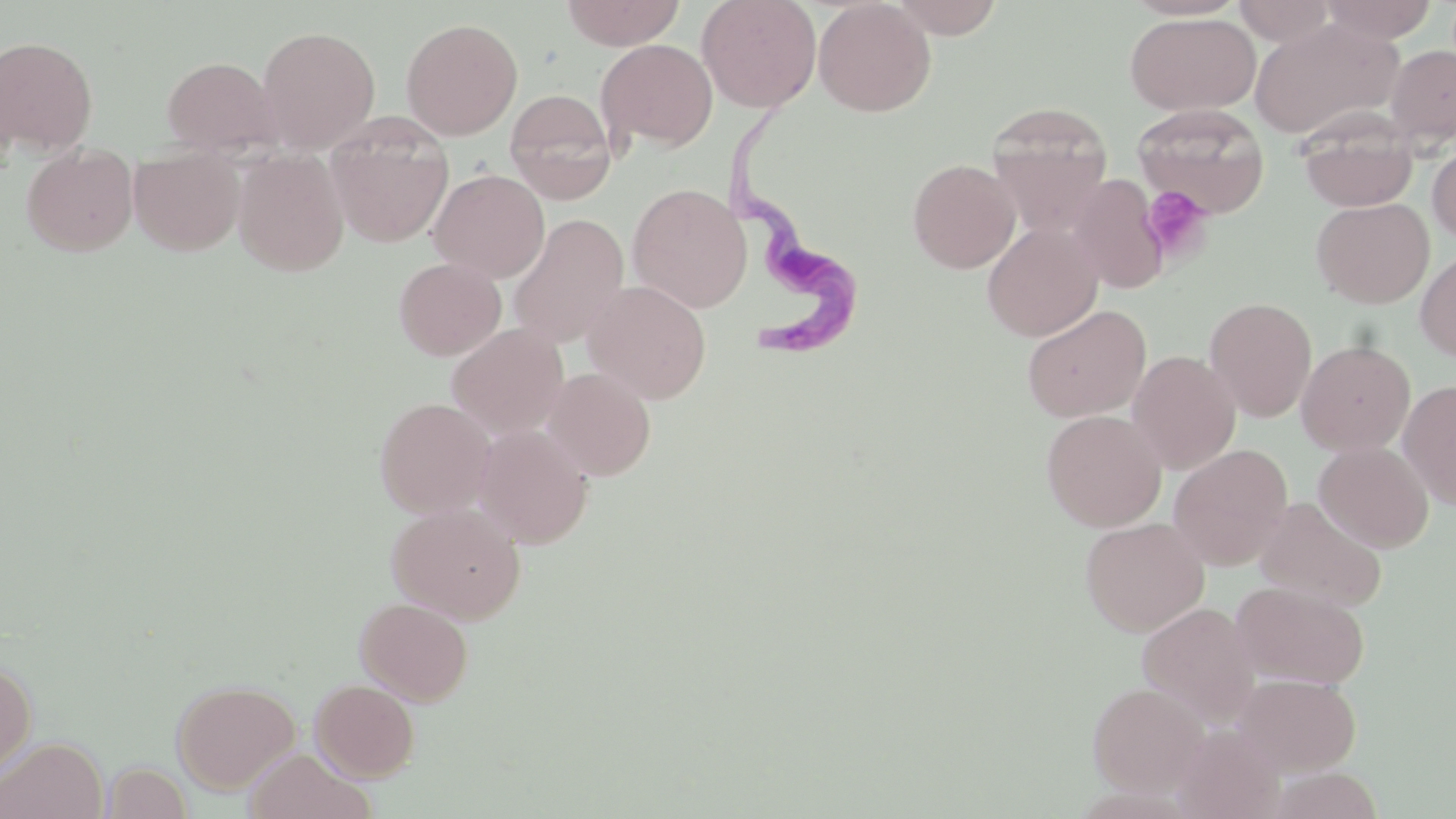
Summary:
  - Coordinate format: approximate bounding boxes as (x1,y1)-(x2,y2) corner pairs in pixels
  - Trypanosoma brucei locations: (720,118)-(870,367)
  - Platelet locations: (1140,184)-(1214,263)
  - Uninfected red blood cell locations: (561,0)-(686,50), (697,0)-(822,113), (813,0)-(936,117), (887,0)-(1006,38), (1231,0)-(1341,45), (1321,0)-(1440,43), (1125,12)-(1260,115), (400,17)-(523,141), (1250,17)-(1403,140), (256,25)-(381,152), (0,37)-(98,153), (596,38)-(718,153), (1386,44)-(1456,145), (0,46)-(24,170), (161,55)-(281,157), (504,88)-(618,204), (986,102)-(1114,231), (1134,103)-(1271,218), (326,117)-(454,248), (1298,119)-(1419,212), (1427,139)-(1456,246), (21,143)-(139,256), (128,145)-(245,255), (233,148)-(349,277), (907,159)-(1020,273), (428,168)-(549,282), (1069,174)-(1169,294), (627,184)-(752,313), (1311,198)-(1434,308), (508,214)-(629,350), (982,221)-(1103,342), (1415,249)-(1456,363), (393,257)-(506,361), (582,280)-(712,404), (1204,297)-(1317,421), (1021,304)-(1152,422), (447,324)-(568,438), (1297,340)-(1416,455), (1127,350)-(1241,474), (542,366)-(656,481), (1398,380)-(1456,510), (374,397)-(495,518), (1041,410)-(1167,531), (473,423)-(594,549), (1313,441)-(1435,552), (1167,444)-(1294,570), (1253,496)-(1386,611), (386,502)-(526,623), (1080,516)-(1210,636), (1231,581)-(1370,689), (355,597)-(474,706), (1137,602)-(1261,726), (0,659)-(36,780), (1233,673)-(1362,775), (311,678)-(420,782), (172,679)-(301,794), (1088,681)-(1210,796), (1173,723)-(1285,819), (0,736)-(107,819), (243,748)-(373,819), (102,761)-(193,819), (1267,766)-(1385,819)
  - Slide-level diagnosis: Trypanosoma brucei
  - Field of view: single
  - Image size: 1456×819 pixels
  - Magnification: 1000x
  - Stain: May-Grünwald-Giemsa
  - Preparation: thin blood film
  - Modality: light microscopy